Find the cells and give the type of each one.
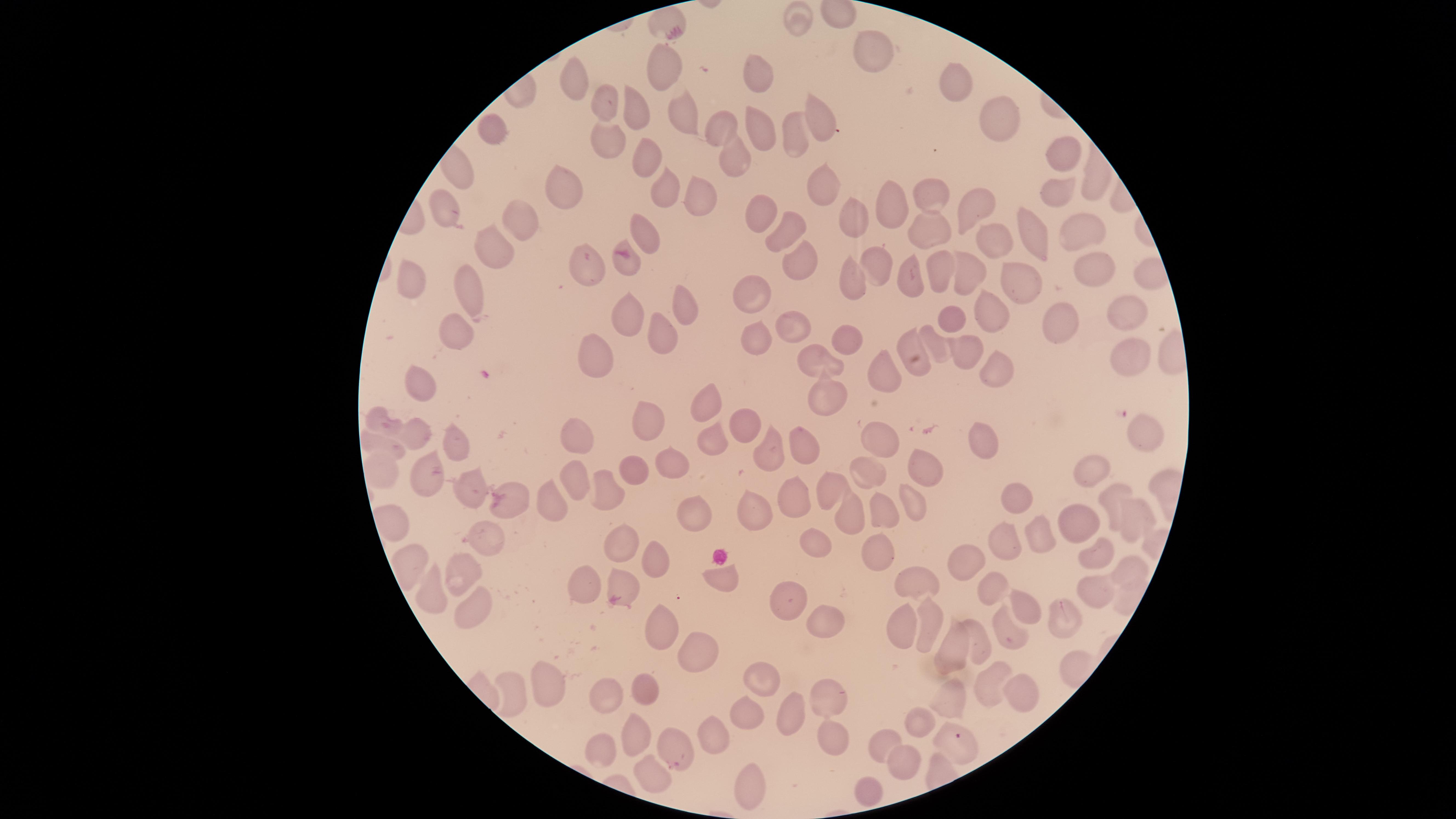

Approximate marker points as (x, y) in pixels.
Parasitized red blood cells: (1060, 606), (673, 764).
Uninfected red blood cells: (663, 18), (801, 22), (869, 52), (662, 69), (762, 72), (577, 77), (960, 79), (604, 105), (638, 109), (819, 117), (1002, 118), (686, 119), (762, 126), (724, 127), (490, 129), (791, 134), (606, 137), (647, 155), (731, 159), (1065, 160), (572, 185), (820, 185), (663, 189), (1059, 189), (934, 190), (696, 196), (884, 200), (977, 202), (452, 208), (761, 213), (853, 213), (526, 218), (932, 228), (1081, 230), (786, 231), (649, 233), (1032, 233), (1001, 235), (496, 248), (805, 262), (877, 263), (583, 264), (943, 266), (1094, 267), (967, 272), (1021, 277), (851, 278), (913, 278), (411, 279), (474, 289), (757, 290), (679, 304), (997, 306), (956, 312), (626, 314), (796, 316), (1127, 317), (1063, 326), (454, 328), (754, 333), (932, 334), (661, 339), (912, 340), (841, 345), (967, 348), (1131, 358), (592, 362), (889, 364), (821, 368), (995, 368), (421, 379), (704, 404), (828, 404), (649, 418), (382, 426), (738, 426), (1141, 428), (413, 431), (580, 434), (880, 438), (382, 440), (710, 440), (978, 440), (804, 442), (456, 443), (770, 444), (669, 465), (1092, 467), (385, 468), (923, 468), (629, 469), (865, 476), (570, 482), (474, 487), (827, 488), (608, 494), (1113, 495), (793, 498), (1018, 498), (548, 500), (508, 505), (692, 507), (886, 507), (914, 507), (752, 510), (851, 520), (1137, 521), (1082, 523), (1045, 536), (620, 538), (1006, 541), (489, 542), (817, 545), (873, 550), (1098, 554), (651, 560), (966, 560), (592, 572), (1129, 574), (461, 576), (920, 579), (723, 582), (986, 586), (626, 591), (1094, 593), (438, 596), (793, 600), (471, 606), (1019, 606), (824, 624), (936, 624), (903, 625), (658, 627), (1012, 631), (983, 637), (954, 645), (705, 657), (769, 677), (989, 679), (549, 680), (1017, 688), (608, 692), (650, 692), (510, 693), (827, 697), (954, 702), (787, 717), (749, 718), (917, 719), (635, 733), (832, 733), (720, 735), (959, 741), (886, 744), (599, 751), (908, 761), (647, 767), (746, 783), (864, 790).
No white blood cells identified.

Smartphone photograph through the microscope eyepiece. Giemsa stain. Image is 1456×819 pixels. Single field of view. Species: Plasmodium falciparum. Circular visible region. Thin blood film.